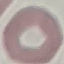 Result: no malaria parasites detected. Acquired by smartphone through the microscope eyepiece. Giemsa-stained preparation. Thin smear of blood. Automatically extracted cell patch, resized to 64 × 64 pixels.